Classify this cell by malaria status.
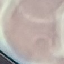
It is uninfected.

Thin blood film. Automatically extracted cell patch, resized to 64 × 64 pixels. Photographed with a smartphone camera at the microscope eyepiece. Giemsa stain.